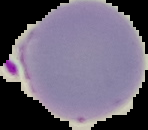
Summary:
  - Image size: 148×130 pixels
  - Malaria status: parasitized
  - Preparation: thin blood film
  - Image type: segmented cell region with the area outside set to black